Assess this cell for malaria.
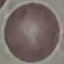

Uninfected.

preparation = thin blood smear
image type = cell patch, automatically extracted from a larger field of view and resized to 64 × 64 pixels
stain = Giemsa
capture = smartphone camera at the microscope eyepiece